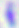
magnification = 400x
modality = micrograph
identification = Toxoplasma gondii